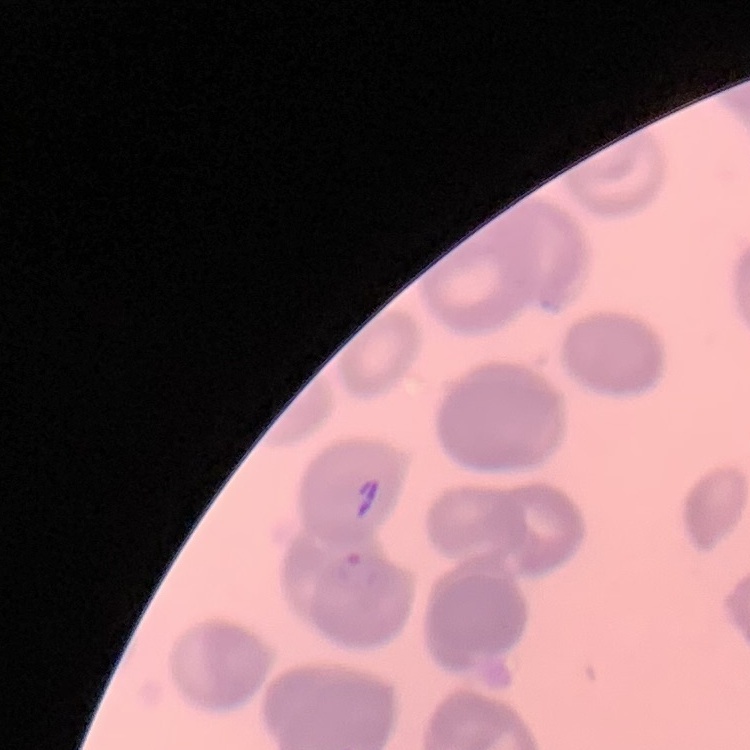
red_blood_cell_morphology: no rouleaux formation
stain: Field's or Giemsa
image_type: square crop of a larger photomicrograph
preparation: thin peripheral smear